Locate every blood parasite and identify its species.
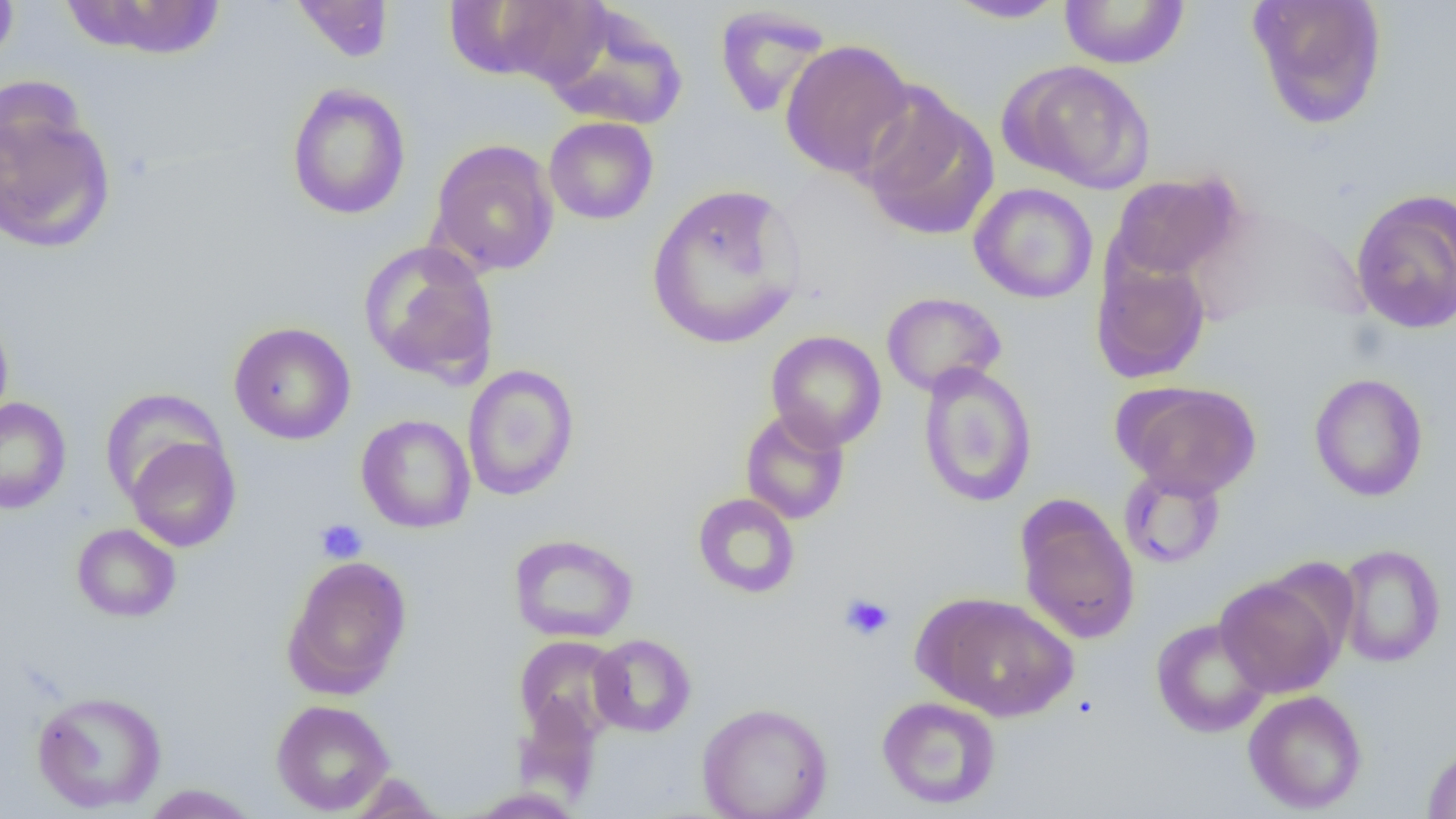
No blood parasites seen.

Approximate bounding boxes as (x1,y1)-(x2,y2) corner pairs in pixels. Uninfected red blood cell locations: (0,0)-(19,71), (61,0)-(227,60), (942,0)-(1071,24), (1059,0)-(1190,69), (1247,0)-(1388,129), (291,1)-(395,63), (452,1)-(608,88), (540,4)-(689,131), (714,5)-(833,119), (779,39)-(917,180), (1002,60)-(1156,194), (286,83)-(411,220), (857,86)-(998,241), (1,94)-(116,255), (544,117)-(658,225), (428,139)-(559,276), (1110,173)-(1242,282), (646,183)-(806,350), (969,183)-(1098,304), (1350,188)-(1456,335), (358,241)-(501,386), (1090,254)-(1211,385), (881,292)-(1006,396), (0,308)-(14,432), (228,321)-(356,445), (765,331)-(887,451), (917,362)-(1038,507), (462,363)-(580,501), (1309,373)-(1429,502), (1117,381)-(1262,498), (99,388)-(226,504), (0,397)-(72,515), (740,407)-(850,525), (356,414)-(476,533), (125,436)-(241,552), (1118,466)-(1226,570), (692,493)-(800,599), (1015,496)-(1140,644), (71,523)-(181,622), (508,533)-(638,643), (1335,544)-(1446,668), (282,554)-(413,698), (1215,576)-(1344,697), (916,592)-(1080,722), (1151,617)-(1271,738), (588,634)-(696,737), (514,635)-(626,741), (31,690)-(167,813), (1243,690)-(1368,814), (876,695)-(1002,810), (513,696)-(603,801), (270,699)-(395,815), (697,702)-(833,819), (1422,744)-(1456,818), (344,773)-(447,818), (139,784)-(262,818). Platelet locations: (315,519)-(367,563), (840,594)-(894,641). Slide-level diagnosis: no evidence of blood parasites. Image is 1456×819 pixels. Captured at 1000x magnification. Single field of view. Thin blood film. Light microscopy.